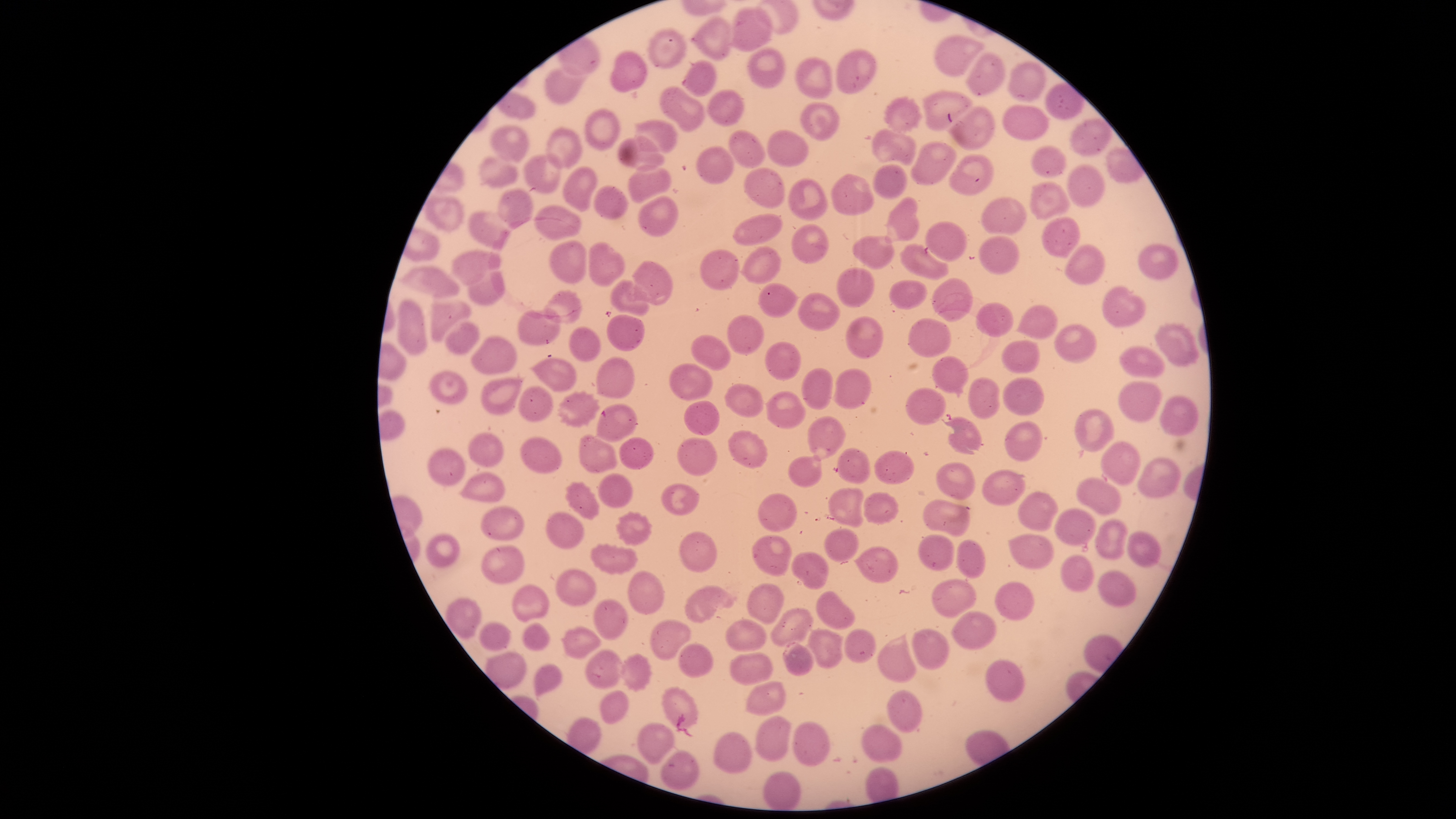

Approximate bounding boxes, in pixels from the top-left corner.
Summary:
  - Uninfected red blood cells: (left=728, top=5, right=774, bottom=51), (left=690, top=14, right=734, bottom=61), (left=646, top=25, right=688, bottom=69), (left=933, top=35, right=986, bottom=78), (left=747, top=47, right=786, bottom=90), (left=835, top=49, right=876, bottom=94), (left=610, top=51, right=648, bottom=93), (left=965, top=51, right=1005, bottom=97), (left=794, top=57, right=832, bottom=100), (left=682, top=60, right=717, bottom=97), (left=1007, top=60, right=1047, bottom=102), (left=545, top=65, right=592, bottom=105), (left=658, top=85, right=706, bottom=133), (left=706, top=89, right=745, bottom=126), (left=922, top=89, right=972, bottom=132), (left=883, top=95, right=923, bottom=134), (left=800, top=101, right=840, bottom=141), (left=1002, top=104, right=1050, bottom=141), (left=945, top=105, right=995, bottom=152), (left=584, top=108, right=620, bottom=151), (left=1069, top=117, right=1112, bottom=157), (left=633, top=118, right=679, bottom=154), (left=489, top=124, right=530, bottom=164), (left=544, top=127, right=584, bottom=170), (left=872, top=128, right=917, bottom=167), (left=727, top=129, right=766, bottom=168), (left=767, top=129, right=811, bottom=167), (left=617, top=135, right=666, bottom=172), (left=911, top=141, right=958, bottom=185), (left=1031, top=143, right=1068, bottom=179), (left=696, top=146, right=735, bottom=185), (left=524, top=153, right=563, bottom=194), (left=477, top=154, right=518, bottom=191), (left=948, top=154, right=996, bottom=195), (left=627, top=163, right=673, bottom=204), (left=873, top=163, right=909, bottom=199), (left=1065, top=163, right=1106, bottom=209), (left=563, top=166, right=598, bottom=212), (left=743, top=167, right=787, bottom=209), (left=831, top=173, right=875, bottom=215), (left=788, top=177, right=830, bottom=221), (left=1029, top=180, right=1072, bottom=221), (left=593, top=185, right=629, bottom=220), (left=496, top=188, right=535, bottom=229), (left=423, top=194, right=465, bottom=232), (left=638, top=194, right=679, bottom=238), (left=884, top=196, right=920, bottom=242), (left=980, top=197, right=1028, bottom=236), (left=534, top=205, right=581, bottom=242), (left=468, top=212, right=512, bottom=251), (left=732, top=214, right=784, bottom=246), (left=1040, top=216, right=1081, bottom=258), (left=925, top=221, right=968, bottom=263), (left=790, top=224, right=830, bottom=266), (left=979, top=235, right=1020, bottom=274), (left=852, top=236, right=895, bottom=270), (left=548, top=241, right=587, bottom=284), (left=587, top=241, right=625, bottom=288), (left=899, top=242, right=949, bottom=281), (left=1064, top=243, right=1106, bottom=286), (left=1137, top=244, right=1179, bottom=281), (left=739, top=247, right=782, bottom=285), (left=699, top=248, right=739, bottom=291), (left=452, top=250, right=502, bottom=286), (left=631, top=260, right=673, bottom=306), (left=397, top=265, right=459, bottom=298), (left=837, top=267, right=874, bottom=309), (left=466, top=270, right=506, bottom=308), (left=931, top=277, right=973, bottom=323), (left=609, top=279, right=651, bottom=317), (left=890, top=279, right=927, bottom=311), (left=758, top=282, right=801, bottom=318), (left=1100, top=285, right=1146, bottom=328), (left=542, top=289, right=583, bottom=325), (left=797, top=292, right=840, bottom=331), (left=396, top=299, right=427, bottom=355), (left=430, top=300, right=474, bottom=341), (left=975, top=302, right=1013, bottom=338), (left=1016, top=304, right=1058, bottom=338), (left=517, top=308, right=562, bottom=345), (left=607, top=314, right=645, bottom=352), (left=728, top=315, right=765, bottom=355), (left=846, top=316, right=883, bottom=360), (left=907, top=317, right=952, bottom=358), (left=444, top=320, right=480, bottom=355), (left=1053, top=323, right=1097, bottom=364), (left=1154, top=323, right=1201, bottom=367), (left=569, top=326, right=601, bottom=362), (left=470, top=335, right=517, bottom=376), (left=691, top=335, right=731, bottom=371), (left=1001, top=340, right=1041, bottom=374), (left=765, top=341, right=802, bottom=381), (left=1117, top=344, right=1166, bottom=378), (left=932, top=355, right=970, bottom=397), (left=597, top=356, right=635, bottom=399), (left=530, top=357, right=577, bottom=392), (left=668, top=363, right=712, bottom=401), (left=801, top=368, right=833, bottom=411), (left=429, top=369, right=468, bottom=405), (left=832, top=369, right=872, bottom=410), (left=481, top=377, right=525, bottom=416), (left=967, top=377, right=1000, bottom=420), (left=1002, top=377, right=1044, bottom=417), (left=1118, top=381, right=1162, bottom=422), (left=724, top=383, right=764, bottom=418), (left=519, top=386, right=554, bottom=424), (left=904, top=388, right=946, bottom=425), (left=764, top=390, right=806, bottom=430), (left=556, top=391, right=600, bottom=429), (left=1159, top=395, right=1200, bottom=437), (left=683, top=400, right=721, bottom=436), (left=595, top=403, right=639, bottom=442), (left=1074, top=409, right=1114, bottom=452), (left=941, top=414, right=984, bottom=455), (left=806, top=416, right=846, bottom=461), (left=1004, top=421, right=1043, bottom=462), (left=728, top=429, right=768, bottom=469), (left=468, top=431, right=505, bottom=468), (left=578, top=434, right=617, bottom=474), (left=519, top=436, right=562, bottom=474), (left=619, top=437, right=654, bottom=470), (left=677, top=437, right=718, bottom=476), (left=1099, top=441, right=1141, bottom=486), (left=427, top=447, right=467, bottom=487), (left=836, top=447, right=872, bottom=485), (left=875, top=450, right=915, bottom=484), (left=788, top=455, right=823, bottom=488), (left=1136, top=456, right=1181, bottom=498), (left=935, top=462, right=976, bottom=499), (left=981, top=468, right=1027, bottom=506), (left=457, top=471, right=506, bottom=502), (left=597, top=472, right=633, bottom=508), (left=1075, top=477, right=1123, bottom=514), (left=564, top=480, right=600, bottom=520), (left=660, top=482, right=701, bottom=515), (left=828, top=487, right=864, bottom=528), (left=1017, top=491, right=1059, bottom=531), (left=863, top=492, right=900, bottom=526), (left=758, top=494, right=795, bottom=532), (left=923, top=499, right=971, bottom=538), (left=480, top=506, right=524, bottom=542), (left=1054, top=507, right=1096, bottom=547), (left=545, top=511, right=586, bottom=549), (left=615, top=511, right=653, bottom=546), (left=1093, top=518, right=1128, bottom=559), (left=823, top=528, right=860, bottom=565), (left=1127, top=529, right=1162, bottom=566), (left=680, top=533, right=716, bottom=573), (left=919, top=533, right=955, bottom=572), (left=1007, top=533, right=1055, bottom=571), (left=425, top=534, right=460, bottom=568), (left=751, top=537, right=791, bottom=576), (left=957, top=538, right=987, bottom=579), (left=590, top=542, right=639, bottom=575), (left=481, top=545, right=525, bottom=585), (left=854, top=546, right=898, bottom=584), (left=791, top=551, right=831, bottom=589), (left=1060, top=555, right=1095, bottom=592), (left=556, top=569, right=598, bottom=608), (left=1097, top=571, right=1136, bottom=606), (left=628, top=572, right=664, bottom=613), (left=931, top=579, right=977, bottom=619), (left=994, top=581, right=1035, bottom=620), (left=512, top=583, right=549, bottom=622), (left=747, top=583, right=785, bottom=625), (left=683, top=585, right=736, bottom=624), (left=816, top=590, right=856, bottom=630), (left=442, top=597, right=481, bottom=641), (left=593, top=598, right=629, bottom=642), (left=770, top=607, right=814, bottom=648), (left=950, top=611, right=997, bottom=649), (left=727, top=620, right=767, bottom=650), (left=478, top=621, right=513, bottom=651), (left=522, top=622, right=551, bottom=652), (left=651, top=622, right=691, bottom=659), (left=561, top=625, right=603, bottom=659), (left=806, top=628, right=845, bottom=669), (left=843, top=628, right=876, bottom=664), (left=912, top=628, right=951, bottom=670), (left=877, top=632, right=918, bottom=683), (left=782, top=641, right=815, bottom=677), (left=678, top=642, right=714, bottom=679), (left=584, top=648, right=622, bottom=689), (left=730, top=652, right=774, bottom=685), (left=620, top=654, right=652, bottom=693), (left=985, top=657, right=1025, bottom=703), (left=534, top=664, right=563, bottom=701), (left=744, top=682, right=787, bottom=717), (left=661, top=686, right=699, bottom=732), (left=599, top=689, right=630, bottom=724), (left=887, top=690, right=923, bottom=734), (left=755, top=716, right=792, bottom=761), (left=792, top=721, right=830, bottom=766), (left=637, top=723, right=675, bottom=764), (left=861, top=724, right=903, bottom=763), (left=713, top=731, right=752, bottom=774), (left=660, top=750, right=700, bottom=791), (left=763, top=770, right=802, bottom=810)
  - Preparation: thin blood smear
  - Field of view: single
  - Image size: 1456×819 pixels
  - Presence: no malaria parasites detected
  - Capture: smartphone photograph through the microscope eyepiece
  - Stain: Giemsa
  - Visible region: circular